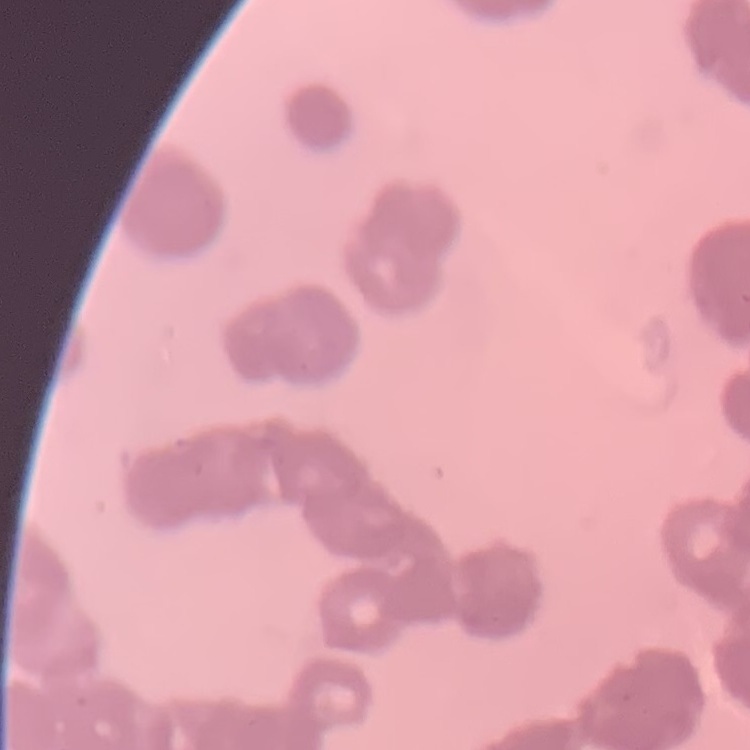
red blood cell morphology = rouleaux formation
preparation = thin peripheral smear
image type = one tile cut from a larger photomicrograph
stain = Field's or Giemsa